Assess the morphology of the erythrocytes.
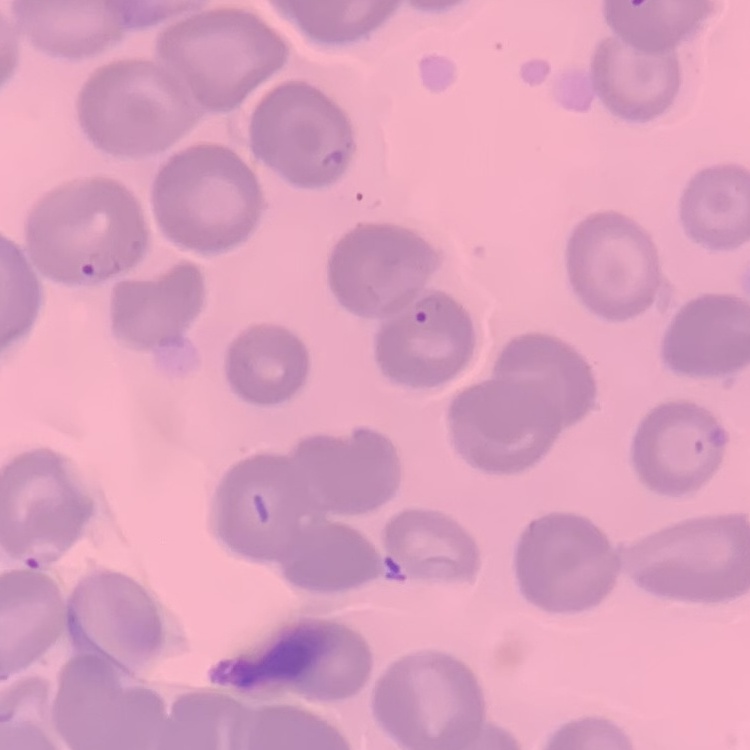

They show no rouleaux formation.

image type = one tile cut from a larger photomicrograph
preparation = thin peripheral smear
stain = Field's or Giemsa